Report the malaria status of this cell.
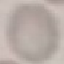

Uninfected.

{
  "image_type": "automatically extracted cell patch, resized to 64 × 64 pixels",
  "stain": "Giemsa",
  "capture": "smartphone camera at the microscope eyepiece",
  "preparation": "thin smear"
}